Assess this cell for malaria.
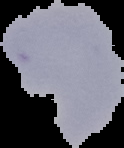

It is uninfected.

{
  "image_size": "124×148 pixels",
  "preparation": "thin blood smear",
  "image_type": "segmented cell region with the area outside set to black"
}